Classify this cell by malaria status.
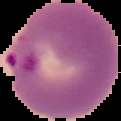

It is parasitized.

Image is 121×121 pixels. From a thin blood smear. The area outside the segmented cell region is set to black.